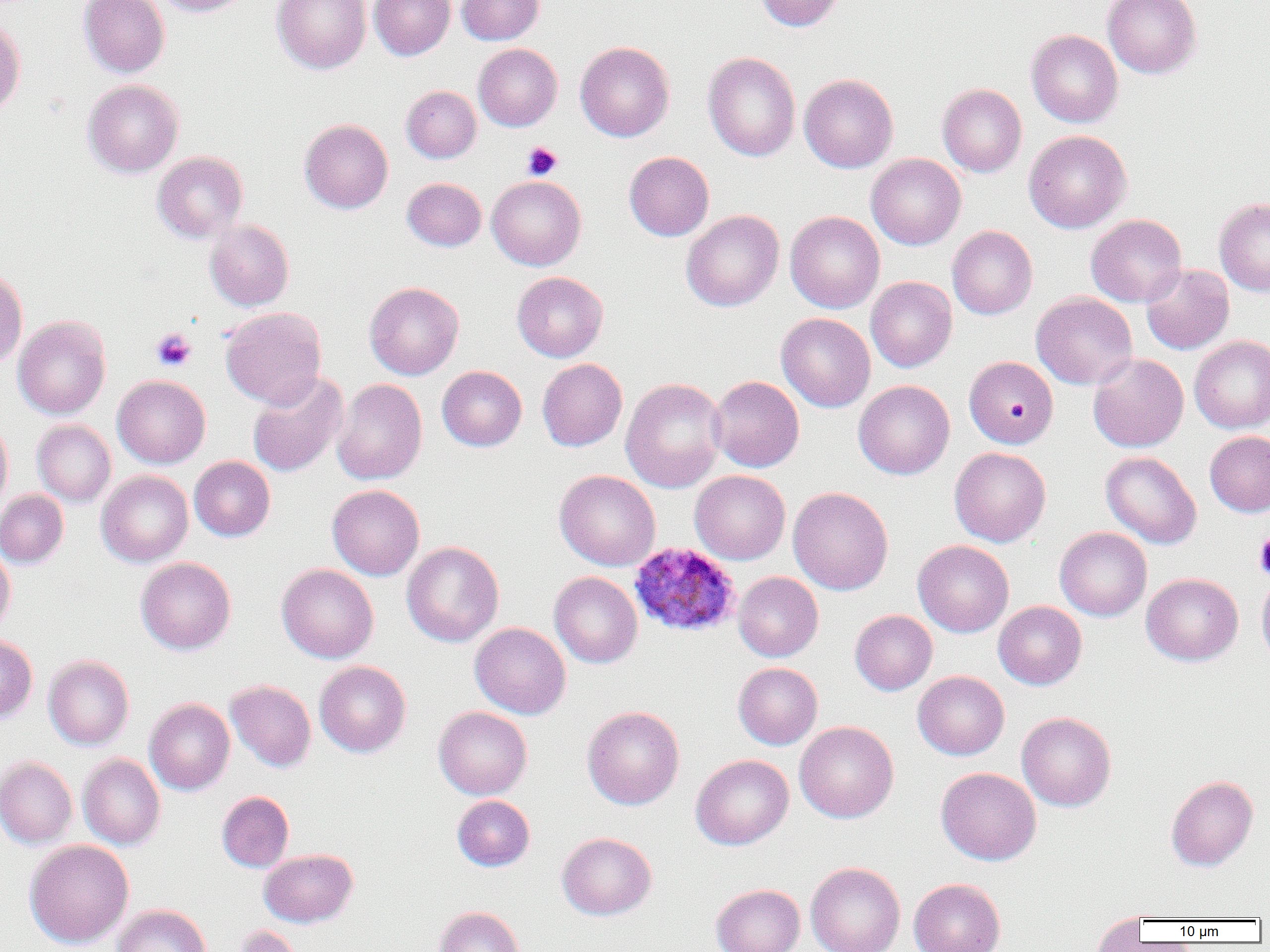
Summary:
  - Coordinate format: approximate bounding boxes as named x1/y1/x2/y2 corners in pixels
  - Plasmodium ovale-infected red blood cell locations: (x1=629, y1=542, x2=740, y2=638)
  - Uninfected red blood cell locations: (x1=78, y1=0, x2=170, y2=77), (x1=152, y1=0, x2=251, y2=17), (x1=272, y1=0, x2=371, y2=74), (x1=370, y1=0, x2=455, y2=60), (x1=457, y1=0, x2=545, y2=45), (x1=755, y1=0, x2=844, y2=31), (x1=1102, y1=0, x2=1202, y2=78), (x1=0, y1=18, x2=26, y2=119), (x1=1026, y1=29, x2=1123, y2=128), (x1=575, y1=41, x2=675, y2=142), (x1=473, y1=43, x2=562, y2=131), (x1=703, y1=52, x2=801, y2=161), (x1=799, y1=73, x2=898, y2=173), (x1=82, y1=79, x2=184, y2=178), (x1=937, y1=83, x2=1027, y2=177), (x1=401, y1=85, x2=481, y2=163), (x1=299, y1=119, x2=393, y2=213), (x1=1024, y1=130, x2=1131, y2=233), (x1=152, y1=151, x2=248, y2=243), (x1=624, y1=151, x2=714, y2=241), (x1=866, y1=153, x2=966, y2=250), (x1=487, y1=175, x2=586, y2=270), (x1=402, y1=177, x2=487, y2=251), (x1=1214, y1=197, x2=1270, y2=296), (x1=681, y1=209, x2=784, y2=311), (x1=785, y1=211, x2=885, y2=313), (x1=1086, y1=214, x2=1187, y2=307), (x1=204, y1=220, x2=294, y2=311), (x1=947, y1=226, x2=1037, y2=320), (x1=1140, y1=264, x2=1234, y2=355), (x1=0, y1=267, x2=28, y2=368), (x1=512, y1=271, x2=608, y2=362), (x1=866, y1=276, x2=957, y2=372), (x1=364, y1=282, x2=464, y2=380), (x1=1031, y1=292, x2=1137, y2=389), (x1=220, y1=307, x2=327, y2=408), (x1=776, y1=312, x2=876, y2=412), (x1=13, y1=316, x2=111, y2=419), (x1=1189, y1=335, x2=1270, y2=432), (x1=1088, y1=354, x2=1188, y2=452), (x1=964, y1=355, x2=1058, y2=448), (x1=537, y1=358, x2=627, y2=451), (x1=437, y1=366, x2=527, y2=451), (x1=246, y1=372, x2=348, y2=477), (x1=112, y1=375, x2=211, y2=468), (x1=709, y1=375, x2=804, y2=472), (x1=621, y1=377, x2=727, y2=493), (x1=331, y1=379, x2=427, y2=485), (x1=853, y1=380, x2=955, y2=479), (x1=0, y1=418, x2=13, y2=515), (x1=32, y1=420, x2=116, y2=506), (x1=1205, y1=430, x2=1270, y2=517), (x1=949, y1=446, x2=1051, y2=547), (x1=1100, y1=451, x2=1202, y2=549), (x1=189, y1=456, x2=275, y2=541), (x1=554, y1=469, x2=660, y2=571), (x1=96, y1=470, x2=193, y2=566), (x1=690, y1=470, x2=790, y2=564), (x1=327, y1=484, x2=425, y2=580), (x1=788, y1=486, x2=893, y2=595), (x1=0, y1=489, x2=69, y2=568), (x1=1055, y1=527, x2=1152, y2=621), (x1=913, y1=540, x2=1014, y2=637), (x1=401, y1=541, x2=504, y2=647), (x1=0, y1=543, x2=15, y2=635), (x1=136, y1=557, x2=236, y2=654), (x1=276, y1=563, x2=379, y2=663), (x1=1256, y1=570, x2=1270, y2=670), (x1=549, y1=572, x2=642, y2=668), (x1=733, y1=572, x2=823, y2=662), (x1=1141, y1=572, x2=1243, y2=666), (x1=993, y1=601, x2=1087, y2=689), (x1=850, y1=610, x2=937, y2=695), (x1=470, y1=622, x2=571, y2=719), (x1=0, y1=634, x2=38, y2=723), (x1=43, y1=655, x2=134, y2=749), (x1=314, y1=660, x2=411, y2=757), (x1=733, y1=662, x2=823, y2=750), (x1=912, y1=671, x2=1009, y2=759), (x1=226, y1=680, x2=316, y2=772), (x1=144, y1=698, x2=235, y2=795), (x1=433, y1=706, x2=532, y2=799), (x1=582, y1=706, x2=684, y2=809), (x1=1017, y1=712, x2=1116, y2=811), (x1=794, y1=721, x2=898, y2=822), (x1=77, y1=754, x2=165, y2=850), (x1=691, y1=754, x2=794, y2=850), (x1=0, y1=756, x2=77, y2=848), (x1=936, y1=767, x2=1041, y2=865), (x1=1166, y1=775, x2=1258, y2=871), (x1=217, y1=791, x2=294, y2=872), (x1=452, y1=795, x2=535, y2=871), (x1=556, y1=832, x2=657, y2=920), (x1=24, y1=839, x2=134, y2=948), (x1=259, y1=849, x2=358, y2=927), (x1=805, y1=861, x2=905, y2=952), (x1=909, y1=878, x2=1006, y2=952), (x1=710, y1=883, x2=805, y2=952), (x1=112, y1=904, x2=211, y2=952), (x1=433, y1=906, x2=525, y2=952), (x1=1090, y1=913, x2=1147, y2=951), (x1=233, y1=925, x2=304, y2=952)
  - Platelet locations: (x1=522, y1=142, x2=562, y2=180), (x1=151, y1=328, x2=197, y2=372), (x1=1254, y1=533, x2=1270, y2=578)
  - Slide-level diagnosis: Plasmodium ovale
  - Field of view: one of a larger specimen
  - Image size: 1270×952 pixels
  - Preparation: thin blood smear
  - Magnification: 1000x
  - Modality: light microscopy